Identify the parasite.
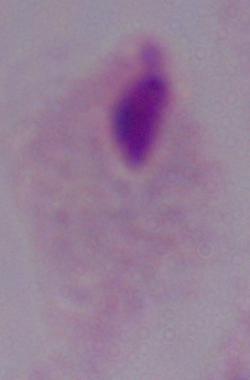
A trichomonad.

Summary:
  - Modality: micrograph
  - Magnification: 1000x